Classify the preparation.
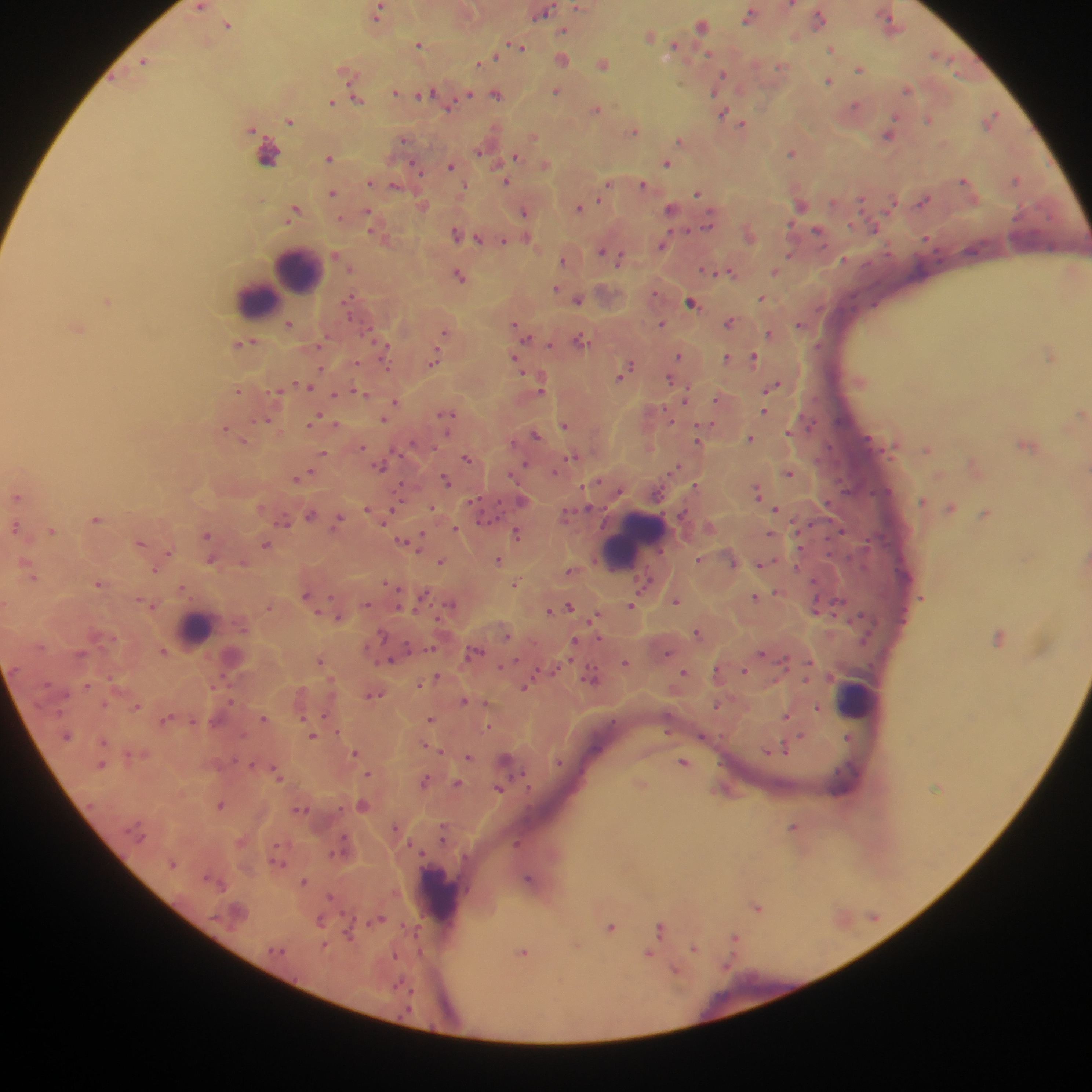

Thick blood smear.

Approximate centers as {x, y} in pixels. Leukocyte locations: {296, 272}, {256, 301}, {633, 542}, {617, 551}, {196, 629}, {856, 698}, {441, 892}. Malaria parasite locations: {792, 5}, {201, 7}, {579, 7}, {378, 13}, {544, 13}, {749, 16}, {819, 18}, {890, 20}, {228, 24}, {702, 26}, {565, 30}, {650, 35}, {420, 45}, {519, 46}, {675, 46}, {832, 49}, {707, 52}, {935, 53}, {494, 56}, {563, 59}, {144, 61}, {480, 63}, {603, 63}, {780, 66}, {859, 69}, {346, 73}, {723, 74}, {719, 80}, {828, 80}, {908, 89}, {556, 91}, {395, 92}, {426, 93}, {469, 94}, {497, 95}, {358, 100}, {332, 102}, {855, 106}, {448, 108}, {597, 109}, {722, 114}, {993, 116}, {893, 118}, {928, 119}, {290, 121}, {743, 124}, {251, 129}, {635, 131}, {889, 135}, {534, 136}, {403, 139}, {681, 140}, {479, 151}, {791, 152}, {266, 153}, {516, 156}, {329, 158}, {546, 164}, {667, 164}, {451, 165}, {418, 170}, {964, 179}, {1017, 179}, {370, 182}, {507, 182}, {643, 184}, {465, 185}, {607, 185}, {395, 186}, {333, 193}, {697, 193}, {861, 199}, {923, 200}, {833, 202}, {800, 204}, {892, 204}, {579, 208}, {671, 209}, {294, 211}, {368, 211}, {524, 211}, {340, 219}, {709, 226}, {874, 228}, {688, 231}, {818, 231}, {456, 233}, {478, 238}, {527, 238}, {927, 238}, {504, 241}, {662, 245}, {601, 250}, {790, 254}, {620, 258}, {844, 259}, {563, 260}, {705, 270}, {712, 271}, {730, 271}, {775, 272}, {459, 275}, {556, 288}, {562, 291}, {655, 292}, {762, 298}, {350, 299}, {578, 299}, {107, 301}, {691, 302}, {349, 314}, {729, 322}, {799, 323}, {289, 324}, {514, 324}, {661, 324}, {77, 328}, {444, 334}, {770, 334}, {526, 338}, {580, 339}, {244, 343}, {550, 344}, {385, 349}, {678, 356}, {1050, 356}, {726, 357}, {753, 358}, {434, 359}, {515, 359}, {629, 365}, {320, 369}, {623, 374}, {670, 378}, {307, 386}, {775, 386}, {541, 389}, {238, 390}, {277, 391}, {360, 392}, {335, 395}, {687, 396}, {717, 400}, {396, 402}, {764, 411}, {1082, 412}, {447, 415}, {315, 419}, {384, 419}, {264, 420}, {335, 425}, {565, 425}, {225, 429}, {790, 431}, {536, 435}, {750, 438}, {244, 440}, {697, 440}, {1024, 445}, {362, 446}, {928, 449}, {323, 454}, {573, 457}, {466, 458}, {525, 465}, {381, 467}, {676, 468}, {789, 473}, {302, 476}, {297, 478}, {445, 479}, {696, 485}, {757, 491}, {16, 497}, {473, 500}, {522, 501}, {922, 501}, {368, 508}, {432, 508}, {588, 508}, {950, 508}, {777, 509}, {985, 514}, {310, 515}, {565, 515}, {96, 519}, {339, 519}, {286, 521}, {15, 527}, {456, 529}, {52, 531}, {841, 531}, {518, 534}, {770, 534}, {207, 535}, {421, 538}, {405, 541}, {141, 543}, {265, 545}, {168, 552}, {699, 559}, {210, 561}, {498, 561}, {441, 562}, {243, 563}, {760, 564}, {797, 565}, {157, 570}, {570, 572}, {33, 577}, {645, 582}, {517, 583}, {98, 584}, {182, 588}, {306, 595}, {756, 597}, {142, 600}, {675, 601}, {149, 604}, {367, 604}, {450, 604}, {632, 605}, {815, 605}, {268, 606}, {569, 606}, {550, 610}, {339, 617}, {596, 618}, {381, 633}, {697, 633}, {999, 637}, {575, 643}, {164, 651}, {474, 652}, {667, 653}, {762, 653}, {391, 659}, {320, 660}, {626, 662}, {502, 666}, {554, 668}, {744, 671}, {684, 672}, {111, 676}, {437, 677}, {593, 678}, {419, 684}, {87, 685}, {526, 686}, {374, 694}, {464, 701}, {137, 706}, {716, 706}, {817, 708}, {325, 715}, {786, 716}, {264, 718}, {430, 718}, {164, 720}, {489, 727}, {67, 736}, {313, 736}, {801, 736}, {702, 737}, {849, 738}, {103, 742}, {785, 749}, {441, 751}, {355, 753}, {468, 756}, {506, 759}, {558, 762}, {684, 762}, {102, 765}, {368, 774}, {278, 775}, {424, 782}, {457, 783}, {499, 789}, {220, 804}, {362, 805}, {395, 826}, {793, 827}, {443, 834}, {517, 843}, {172, 864}, {528, 879}, {304, 882}, {330, 896}, {757, 907}, {380, 919}, {874, 919}, {320, 920}, {611, 927}, {661, 929}, {416, 931}, {348, 934}, {735, 941}, {694, 949}, {524, 953}, {648, 954}, {394, 956}, {675, 971}. Collected in Ghana. Image is 1092×1092 pixels. One field of view. Mobile-phone photograph taken through the microscope.